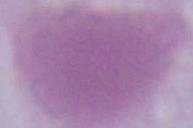
Captured at 1000x magnification. A red blood cell is seen. Photomicrograph.